Name the parasite shown.
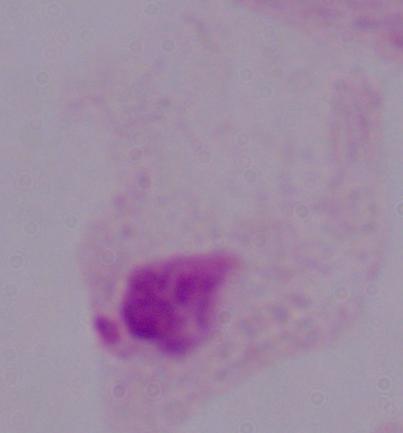
This is a trichomonad.

modality: micrograph
magnification: 1000x